Point out leukocytes.
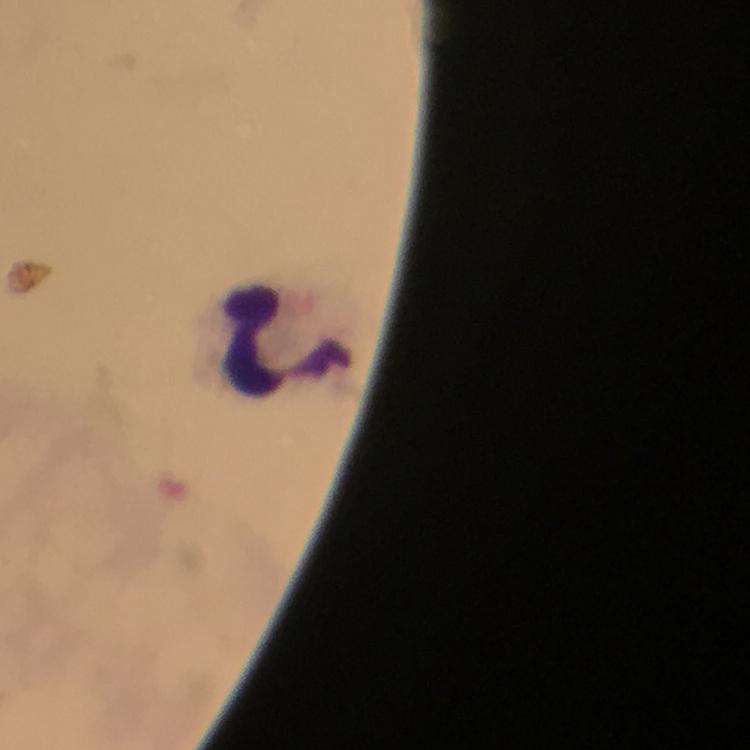

Approximate centers as (x, y) in pixels.
Leukocytes: (287, 339).

preparation = thick smear
stain = Giemsa
context = from a diagnostic examination for malaria
capture = smartphone photograph through a microscope
immersion oil = applied
magnification = 100x
cropped from = a single field of view
malaria parasites = none seen
image size = 750×750 pixels